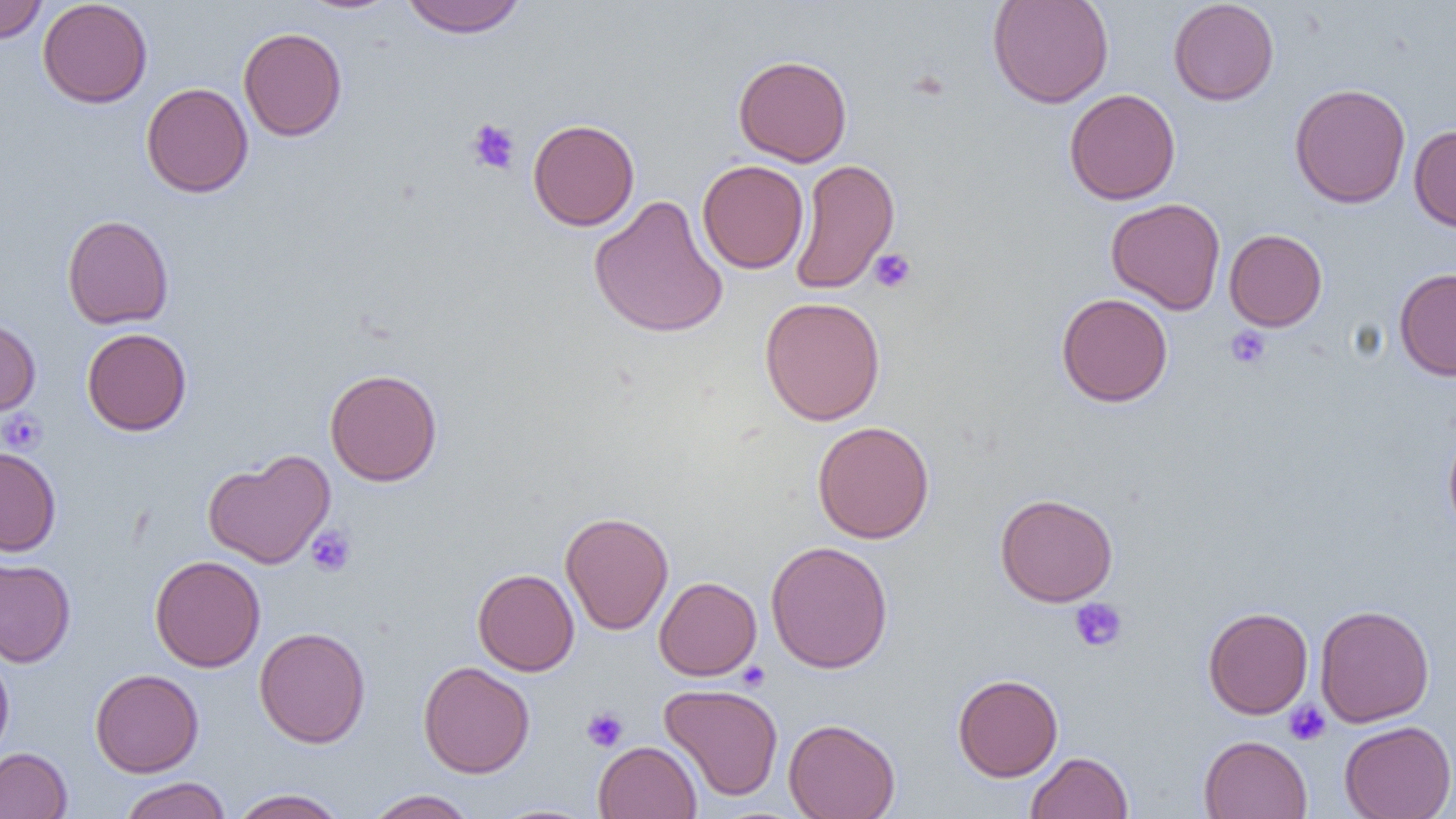
Approximate bounding boxes as (x1,y1)-(x2,y2) corner pairs in pixels. Uninfected red blood cell locations: (0,0)-(48,44), (38,0)-(153,108), (296,0)-(403,15), (399,0)-(528,38), (987,0)-(1114,109), (1167,0)-(1280,106), (238,26)-(347,141), (733,54)-(852,167), (141,82)-(253,198), (1289,83)-(1411,208), (1064,88)-(1181,205), (527,118)-(640,231), (1409,124)-(1456,233), (789,158)-(900,295), (697,159)-(809,274), (588,195)-(729,339), (1106,197)-(1226,314), (62,214)-(174,330), (1224,229)-(1327,331), (1394,268)-(1456,380), (1056,292)-(1173,407), (759,296)-(886,425), (0,317)-(41,417), (82,328)-(192,435), (324,368)-(443,486), (812,421)-(935,544), (1443,427)-(1456,538), (0,447)-(61,557), (203,449)-(336,569), (994,492)-(1118,607), (560,511)-(674,635), (766,540)-(894,673), (150,555)-(266,672), (0,557)-(76,667), (473,568)-(580,676), (654,576)-(762,680), (1314,604)-(1434,727), (1203,606)-(1313,719), (254,626)-(371,748), (0,651)-(14,763), (418,661)-(535,778), (90,668)-(204,777), (952,674)-(1064,781), (659,683)-(784,801), (783,717)-(901,819), (1339,720)-(1456,819), (1198,734)-(1312,818), (593,740)-(702,819), (0,747)-(72,818), (1025,751)-(1133,819), (118,777)-(232,819), (229,788)-(348,819), (364,789)-(478,818). Platelet locations: (465,118)-(520,175), (868,248)-(917,294), (1224,326)-(1272,370), (0,410)-(47,454), (306,526)-(357,577), (1069,598)-(1128,652), (737,661)-(771,691), (1283,700)-(1331,746), (582,706)-(628,752). Slide-level diagnosis: negative for blood parasites. Image is 1456×819 pixels. Thin blood film. One field of a larger specimen. Light microscopy. 1000x magnification.